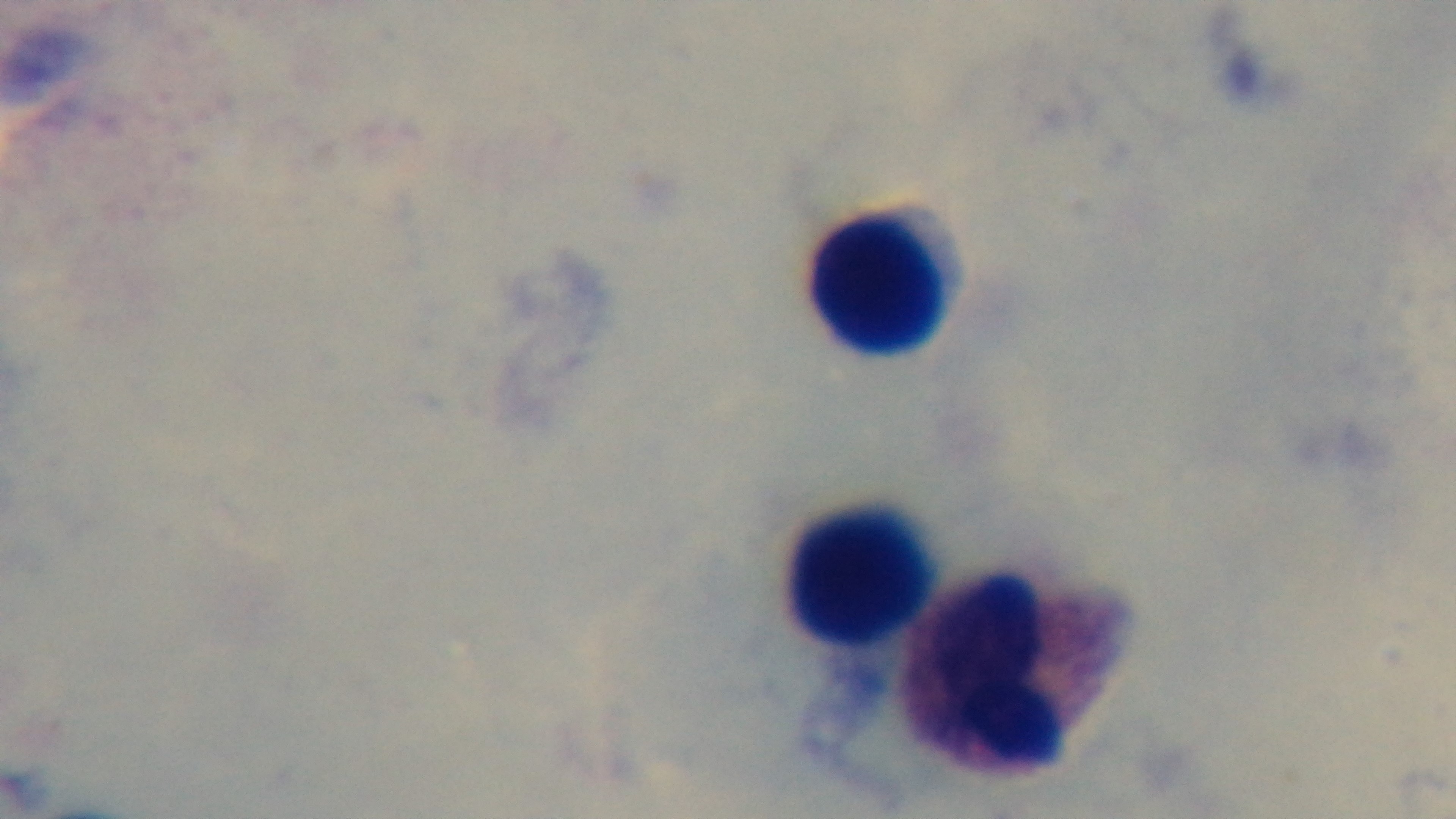
Preparation: thick blood film. Giemsa-stained. Light microscopy. Captured with a mounted 4K digital camera. Oil-immersion objective, 100x. One field from the slide. Malaria status: negative.